Assess this cell for malaria.
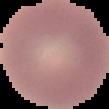
It is uninfected.

From a thin blood film. Cell region segmented out of the field of view; the surrounding area is masked to black. Image is 109×109 pixels.